Give the location of every parasitized red blood cell.
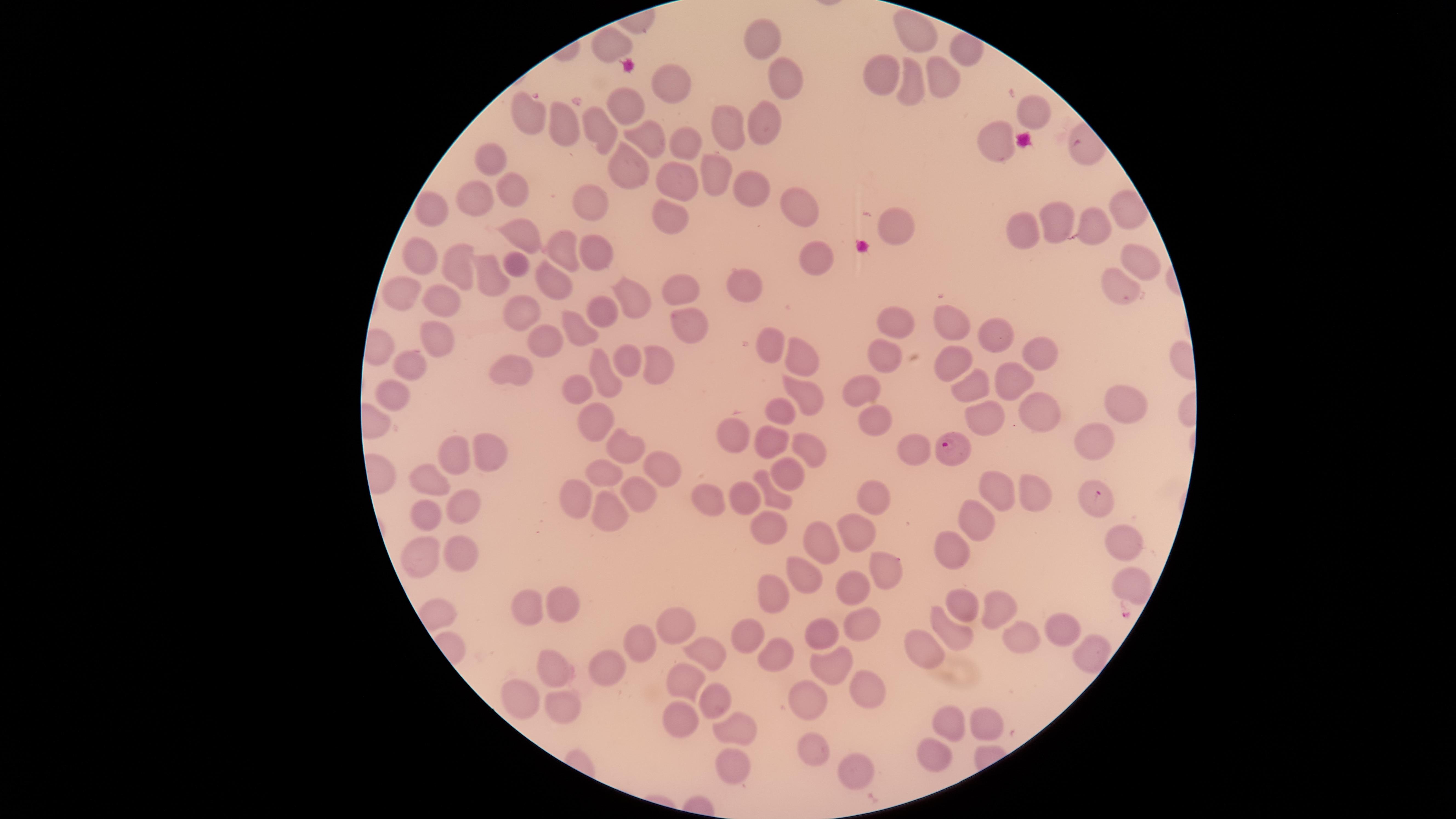

Approximate marker points, in pixels from the top-left corner.
Parasitized red blood cells: (x=949, y=448), (x=1098, y=499).

visible_region: circular
species: Plasmodium falciparum
uninfected_red_blood_cells: 'approximate marker points, in pixels from the top-left corner: (x=921, y=32), (x=764, y=34), (x=780, y=75), (x=878, y=75), (x=940, y=75), (x=913, y=84), (x=666, y=86), (x=625, y=107), (x=1032, y=111), (x=517, y=119), (x=563, y=122), (x=769, y=123), (x=729, y=124), (x=602, y=125), (x=654, y=136), (x=683, y=139), (x=999, y=141), (x=496, y=163), (x=623, y=165), (x=718, y=171), (x=670, y=176), (x=511, y=188), (x=749, y=189), (x=478, y=197), (x=593, y=204), (x=788, y=205), (x=435, y=207), (x=668, y=216), (x=1057, y=219), (x=895, y=224), (x=1091, y=228), (x=1026, y=230), (x=517, y=233), (x=596, y=244), (x=561, y=249), (x=424, y=253), (x=1130, y=259), (x=823, y=263), (x=519, y=267), (x=453, y=268), (x=673, y=281), (x=492, y=283), (x=558, y=285), (x=409, y=288), (x=1117, y=288), (x=751, y=289), (x=441, y=290), (x=640, y=297), (x=602, y=309), (x=529, y=313), (x=892, y=313), (x=690, y=321), (x=947, y=322), (x=437, y=327), (x=575, y=331), (x=992, y=335), (x=546, y=343), (x=1033, y=347), (x=768, y=348), (x=806, y=356), (x=624, y=360), (x=655, y=360), (x=890, y=360), (x=947, y=365), (x=409, y=368), (x=520, y=370), (x=600, y=377), (x=1015, y=379), (x=576, y=382), (x=867, y=386), (x=976, y=386), (x=400, y=391), (x=809, y=392), (x=1127, y=403), (x=781, y=408), (x=1047, y=414), (x=876, y=415), (x=983, y=419), (x=601, y=422), (x=740, y=431), (x=767, y=442), (x=621, y=446), (x=1099, y=446), (x=461, y=447), (x=911, y=451), (x=813, y=452), (x=485, y=455), (x=663, y=467), (x=600, y=470), (x=438, y=473), (x=787, y=477), (x=993, y=485), (x=1028, y=487), (x=869, y=493), (x=749, y=494), (x=571, y=498), (x=774, y=498), (x=629, y=501), (x=711, y=501), (x=469, y=502), (x=421, y=514), (x=970, y=514), (x=601, y=516), (x=766, y=527), (x=853, y=533), (x=820, y=540), (x=1120, y=540), (x=950, y=544), (x=421, y=550), (x=464, y=551), (x=873, y=566), (x=803, y=577), (x=1127, y=585), (x=776, y=587), (x=846, y=587), (x=562, y=601), (x=527, y=606), (x=968, y=608), (x=997, y=608), (x=672, y=626), (x=860, y=626), (x=1065, y=627), (x=746, y=631), (x=823, y=632), (x=945, y=632), (x=1024, y=640), (x=640, y=644), (x=923, y=644), (x=712, y=646), (x=778, y=646), (x=1091, y=649), (x=550, y=663), (x=609, y=665), (x=826, y=665), (x=688, y=673), (x=860, y=693), (x=810, y=695), (x=711, y=701), (x=515, y=702), (x=560, y=705), (x=670, y=712), (x=992, y=712), (x=950, y=722), (x=733, y=729), (x=811, y=744), (x=937, y=753), (x=736, y=768), (x=848, y=771)'
field_of_view: single
stain: Giemsa
capture: smartphone photograph through the microscope eyepiece
image_size: 1456×819 pixels
preparation: thin blood smear